Assess the morphology of the red blood cells.
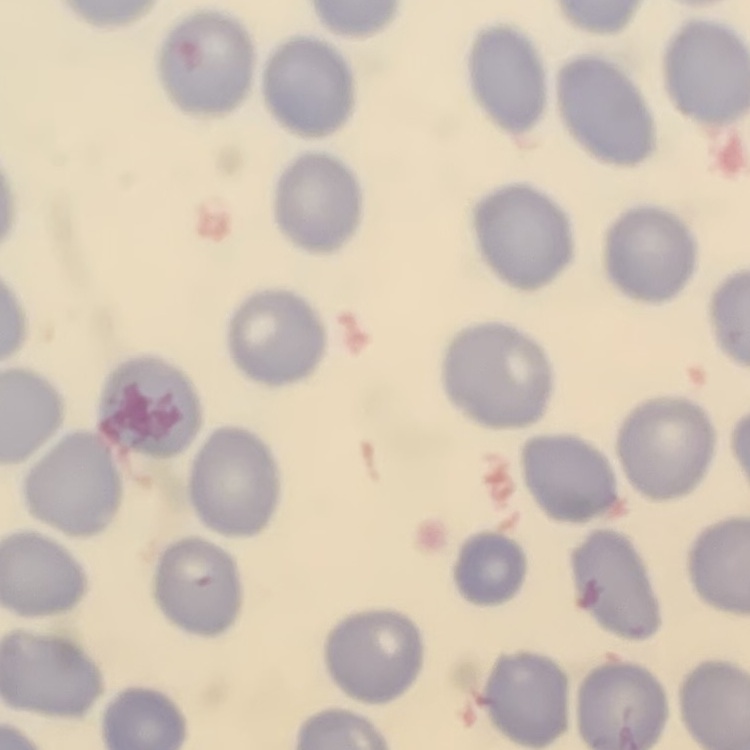

No rouleaux formation.

Summary:
  - Preparation: thin peripheral smear
  - Stain: Field's or Giemsa
  - Image type: square crop of a larger photomicrograph